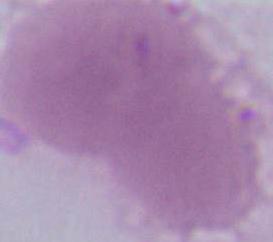
Summary:
  - Modality: photomicrograph
  - Identification: erythrocyte
  - Magnification: 1000x